Report the malaria status of this cell.
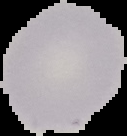

Uninfected.

From a thin blood smear. Image is 127×136 pixels. Cell region segmented out of the field of view; the surrounding area is masked to black.